Describe the morphology of the red blood cells.
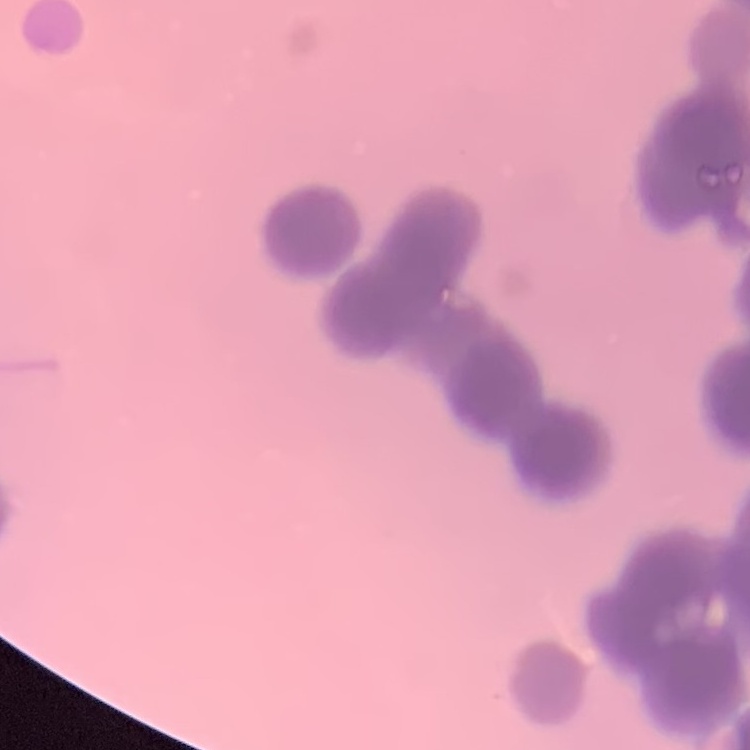
Rouleaux formation.

image type = one tile cut from a larger photomicrograph
stain = Field's or Giemsa
preparation = thin blood film